Assess this cell for malaria.
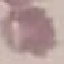

It is uninfected.

Cell patch, automatically extracted from a larger field of view and resized to 64 × 64 pixels. Thin blood film. Acquired by smartphone through the microscope eyepiece. Giemsa stain.